Locate leukocytes (white blood cells).
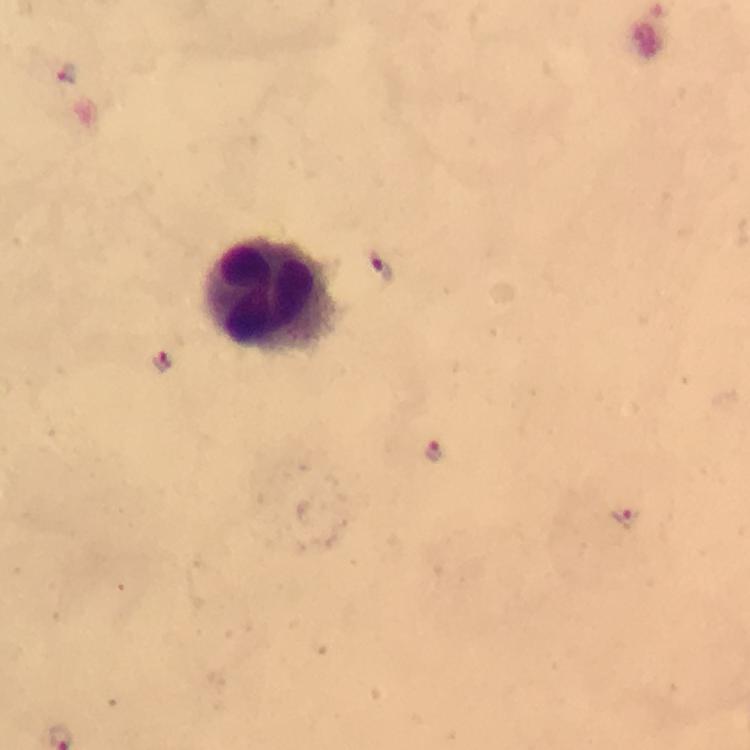
Approximate centers as (x, y) in pixels.
Leukocytes: (274, 294).

Plasmodium parasite locations: (69, 76), (382, 266), (160, 363), (436, 451), (624, 517). From a malaria diagnostic workup. Giemsa stain. A crop from one field of view. 100x magnification. Thick blood smear. Immersion oil was used. Image is 750×750 pixels. Photographed with a smartphone mounted on the microscope.